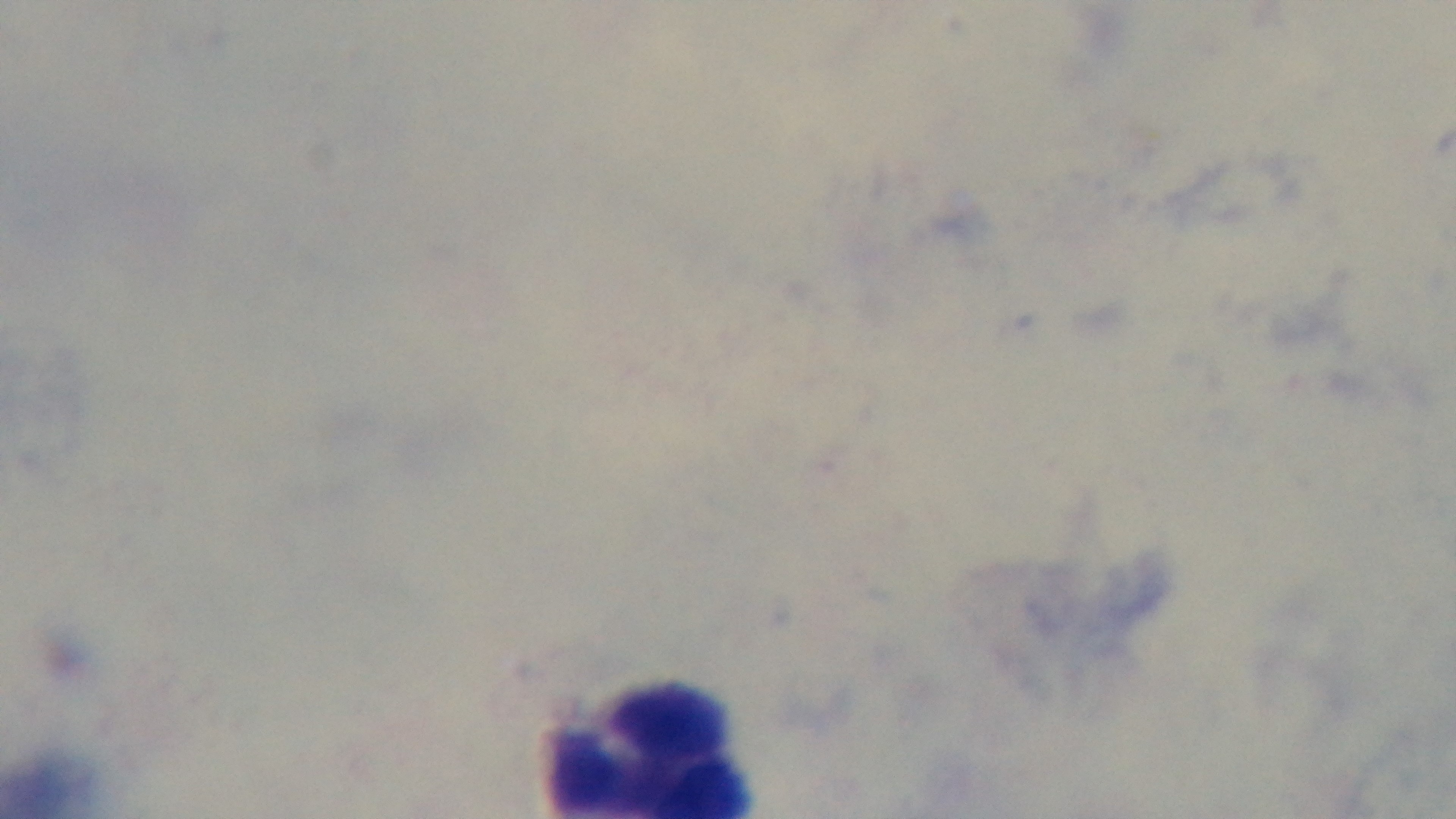
Summary:
  - Preparation: thick blood film
  - Stain: Giemsa
  - Modality: light microscopy
  - Capture: mounted 4K digital camera
  - Field of view: single
  - Objective: 100x oil immersion
  - Malaria status: uninfected